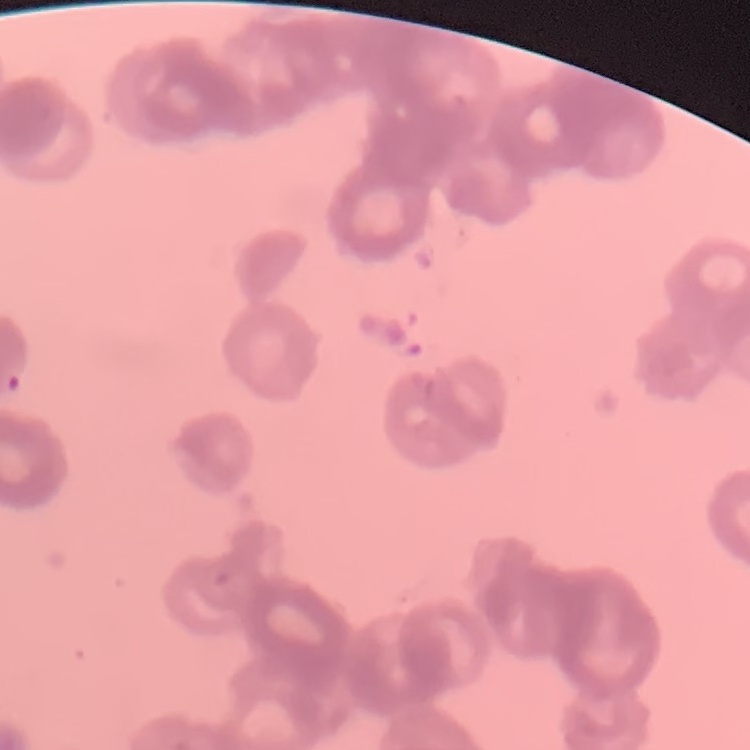

red blood cell morphology = rouleaux formation
preparation = thin blood film
image type = square crop of a larger photomicrograph
stain = Field's or Giemsa